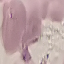

{
  "result": "no malaria parasites seen",
  "preparation": "thin blood film",
  "capture": "smartphone through the microscope eyepiece",
  "stain": "Giemsa",
  "image_type": "automatically extracted cell patch, resized to 64 × 64 pixels"
}